Classify this cell by malaria status.
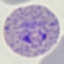
Parasitized.

preparation = thin smear
stain = Giemsa
capture = smartphone camera at the microscope eyepiece
image type = cell patch, automatically extracted from a larger field of view and resized to 64 × 64 pixels